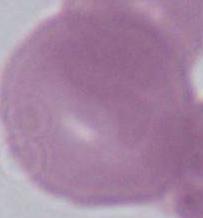
Photomicrograph. A red blood cell is seen. 1000x magnification.